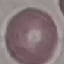

result = no malaria parasites detected
preparation = thin smear
stain = Giemsa
image type = cell patch, automatically extracted from a larger field of view and resized to 64 × 64 pixels
capture = smartphone camera at the microscope eyepiece